State the blood parasite species.
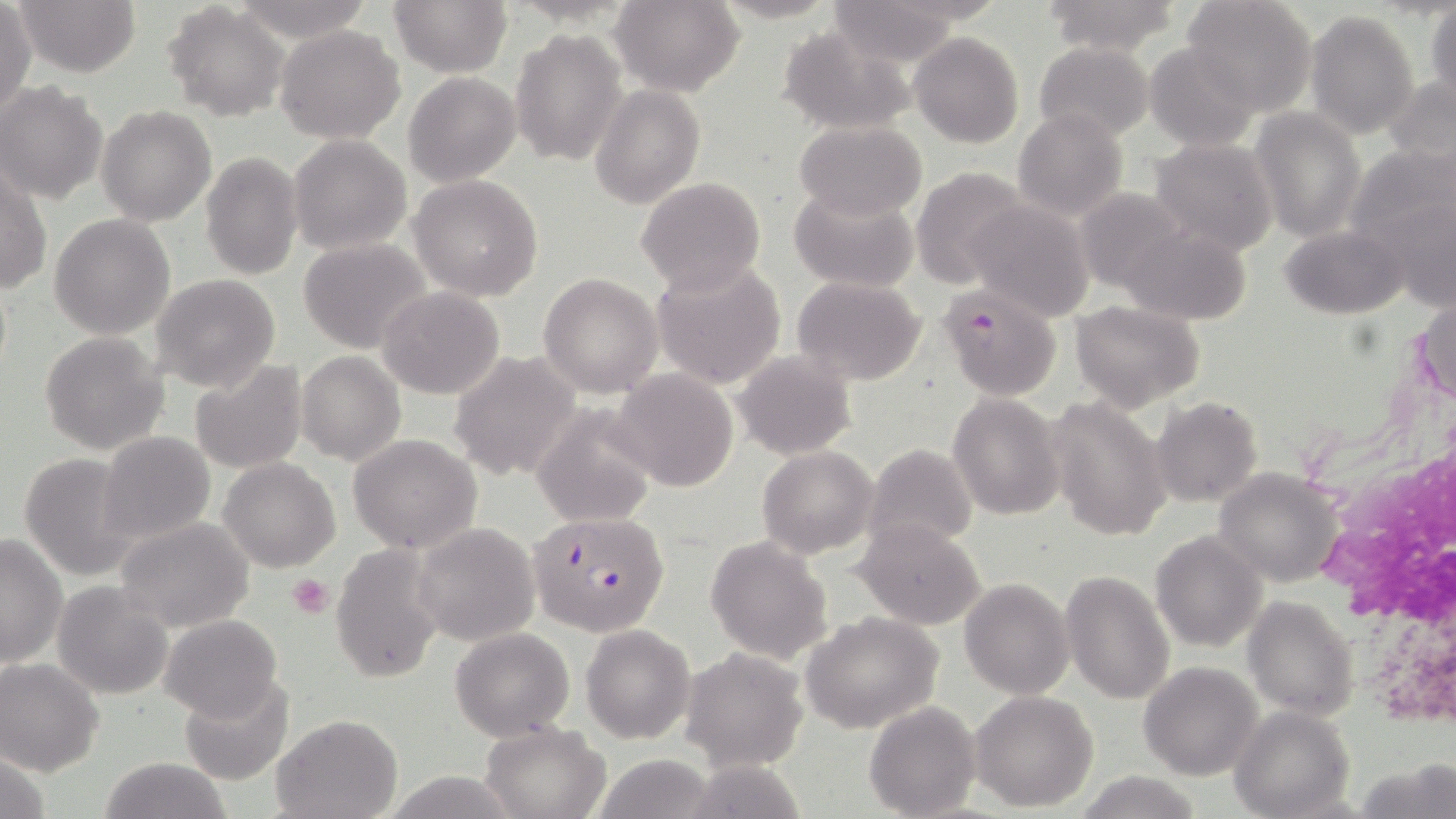
Plasmodium falciparum.

Summary:
  - Coordinate format: approximate bounding boxes as (x1,y1)-(x2,y2) corner pairs in pixels
  - Plasmodium falciparum-infected red blood cell locations: (939,285)-(1062,397), (528,510)-(670,636)
  - Platelet locations: (287,572)-(336,619)
  - White blood cell locations: (1314,308)-(1456,749)
  - Uninfected red blood cell locations: (14,0)-(142,77), (233,0)-(374,41), (389,0)-(510,76), (611,0)-(745,96), (707,0)-(843,24), (1037,0)-(1182,56), (1179,0)-(1317,114), (821,2)-(966,66), (0,3)-(35,117), (165,3)-(289,119), (1426,4)-(1456,101), (1305,10)-(1419,139), (775,23)-(918,136), (275,25)-(405,145), (510,28)-(628,168), (909,32)-(1025,148), (1035,41)-(1155,145), (1145,42)-(1262,152), (404,72)-(520,186), (1384,74)-(1456,170), (0,81)-(110,204), (590,84)-(704,208), (97,104)-(215,225), (1012,108)-(1128,221), (1248,108)-(1366,242), (794,119)-(926,221), (287,134)-(411,255), (1148,137)-(1280,257), (1348,140)-(1455,272), (199,150)-(303,282), (1,167)-(50,295), (911,168)-(1032,288), (410,174)-(544,301), (635,177)-(766,296), (789,184)-(920,295), (1073,186)-(1194,295), (962,198)-(1095,320), (49,214)-(176,340), (1116,221)-(1255,324), (1278,223)-(1405,319), (297,237)-(434,353), (650,259)-(787,390), (538,273)-(663,397), (150,274)-(281,392), (791,276)-(927,385), (378,286)-(506,400), (1070,300)-(1206,412), (40,332)-(169,456), (297,350)-(406,466), (733,350)-(856,459), (449,353)-(582,481), (190,359)-(308,474), (612,368)-(738,492), (948,394)-(1065,519), (1151,396)-(1263,507), (1048,397)-(1171,543), (531,404)-(659,529), (96,431)-(216,548), (348,434)-(482,554), (863,443)-(977,557), (757,446)-(879,557), (18,452)-(141,580), (219,457)-(341,572), (1212,467)-(1346,588), (116,516)-(255,632), (851,518)-(986,633), (410,522)-(541,646), (1151,530)-(1268,652), (1,533)-(68,669), (705,535)-(834,665), (332,543)-(448,684), (1060,570)-(1175,704), (959,577)-(1074,699), (52,582)-(174,699), (1243,595)-(1360,720), (801,611)-(945,734), (159,614)-(284,722), (580,623)-(695,742), (450,628)-(576,740), (681,646)-(811,770), (0,658)-(104,775), (1138,661)-(1263,780), (180,675)-(294,786), (970,689)-(1099,811), (865,701)-(980,817), (1230,706)-(1354,818), (271,712)-(402,818), (479,720)-(611,819), (587,752)-(723,819), (100,755)-(232,819), (383,772)-(525,817), (1074,772)-(1204,818)
  - Field of view: one of a larger specimen
  - Modality: light microscopy
  - Magnification: 1000x
  - Image size: 1456×819 pixels
  - Stain: May-Grünwald-Giemsa
  - Preparation: thin blood smear